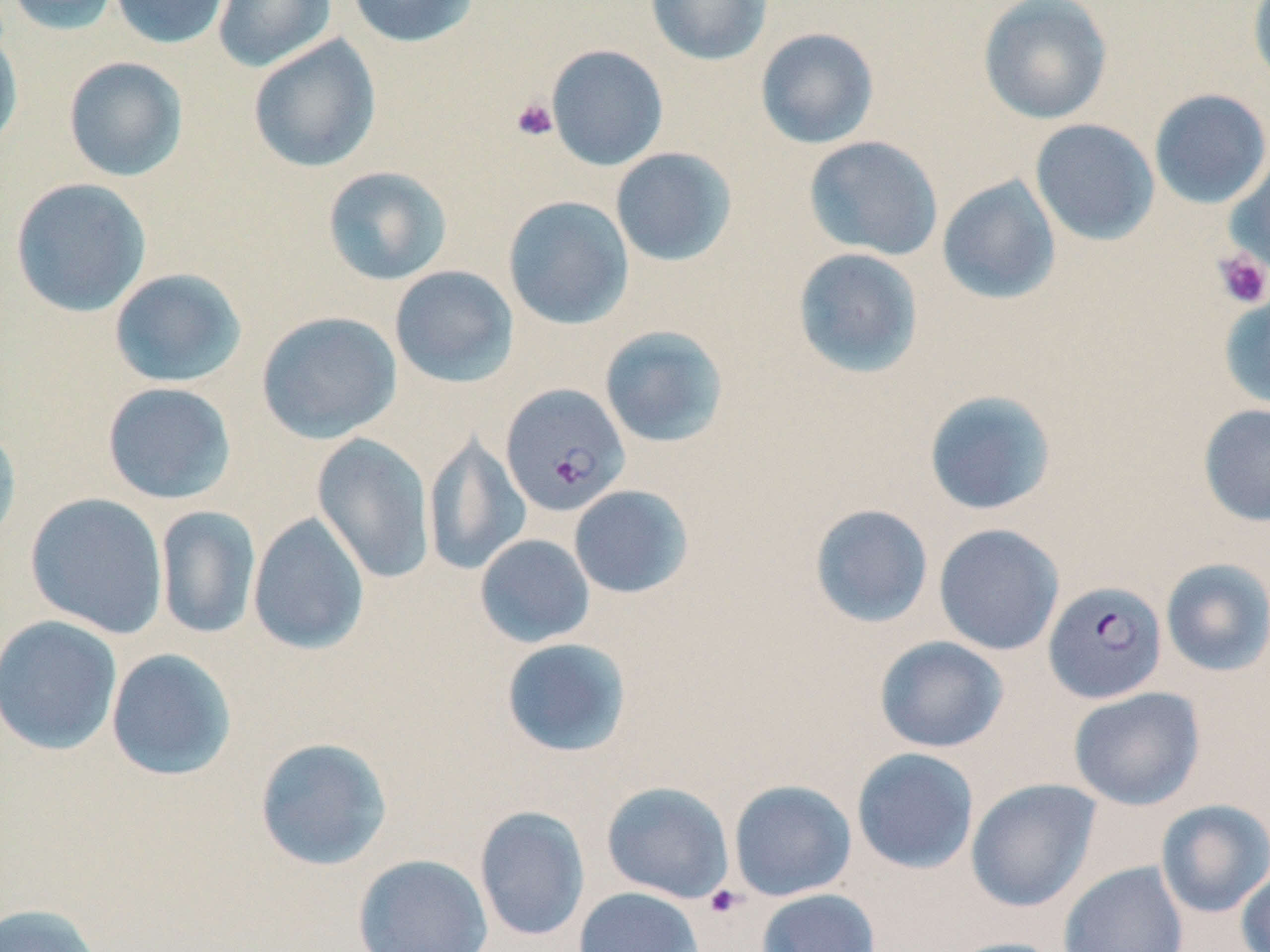

slide_level_diagnosis: Plasmodium falciparum
platelet_locations: 'approximate bounding boxes as [x1, y1, x2, y2] in pixels: [511, 97, 558, 141], [1213, 250, 1270, 309], [704, 884, 745, 918]'
magnification: 1000x
modality: optical microscopy
uninfected_red_blood_cell_locations: 'approximate bounding boxes as [x1, y1, x2, y2] in pixels: [5, 0, 122, 36], [109, 0, 231, 49], [213, 0, 336, 72], [347, 0, 480, 48], [645, 0, 773, 66], [978, 0, 1113, 124], [1247, 0, 1270, 93], [0, 27, 23, 154], [755, 27, 879, 149], [247, 34, 381, 173], [546, 44, 669, 171], [62, 56, 189, 182], [1149, 88, 1270, 209], [1030, 118, 1159, 245], [803, 136, 944, 261], [610, 147, 737, 267], [1226, 153, 1270, 275], [322, 166, 452, 286], [936, 175, 1062, 306], [10, 178, 152, 317], [503, 195, 634, 330], [792, 247, 924, 378], [389, 265, 519, 388], [109, 268, 247, 389], [1218, 292, 1270, 410], [256, 311, 402, 444], [599, 325, 730, 448], [102, 382, 237, 505], [922, 390, 1058, 517], [1198, 403, 1270, 527], [0, 423, 22, 552], [423, 432, 530, 577], [312, 433, 435, 583], [568, 485, 694, 599], [25, 492, 169, 640], [809, 503, 934, 629], [155, 505, 261, 640], [248, 512, 370, 655], [933, 523, 1065, 656], [475, 533, 595, 648], [1160, 558, 1270, 677], [0, 614, 123, 756], [873, 636, 1009, 753], [500, 637, 632, 758], [105, 647, 237, 782], [1068, 686, 1205, 810], [254, 737, 393, 871], [851, 747, 980, 874], [965, 778, 1101, 913], [728, 779, 857, 901], [601, 781, 735, 903], [1156, 799, 1270, 918], [474, 805, 590, 943], [352, 853, 493, 951], [1059, 861, 1189, 952], [1236, 866, 1270, 952], [573, 887, 704, 952], [756, 888, 881, 952], [0, 902, 103, 952], [943, 937, 1067, 952]'
preparation: thin blood film
stain: May-Grünwald-Giemsa
field_of_view: one of a larger specimen
plasmodium_falciparum_infected_red_blood_cell_locations: 'approximate bounding boxes as [x1, y1, x2, y2] in pixels: [501, 383, 629, 517], [1043, 580, 1167, 704]'
image_size: 1270×952 pixels